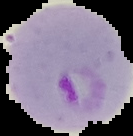
Image is 133×136 pixels. Result: Plasmodium parasites detected. Segmented cell region on a black background. From a thin blood film.